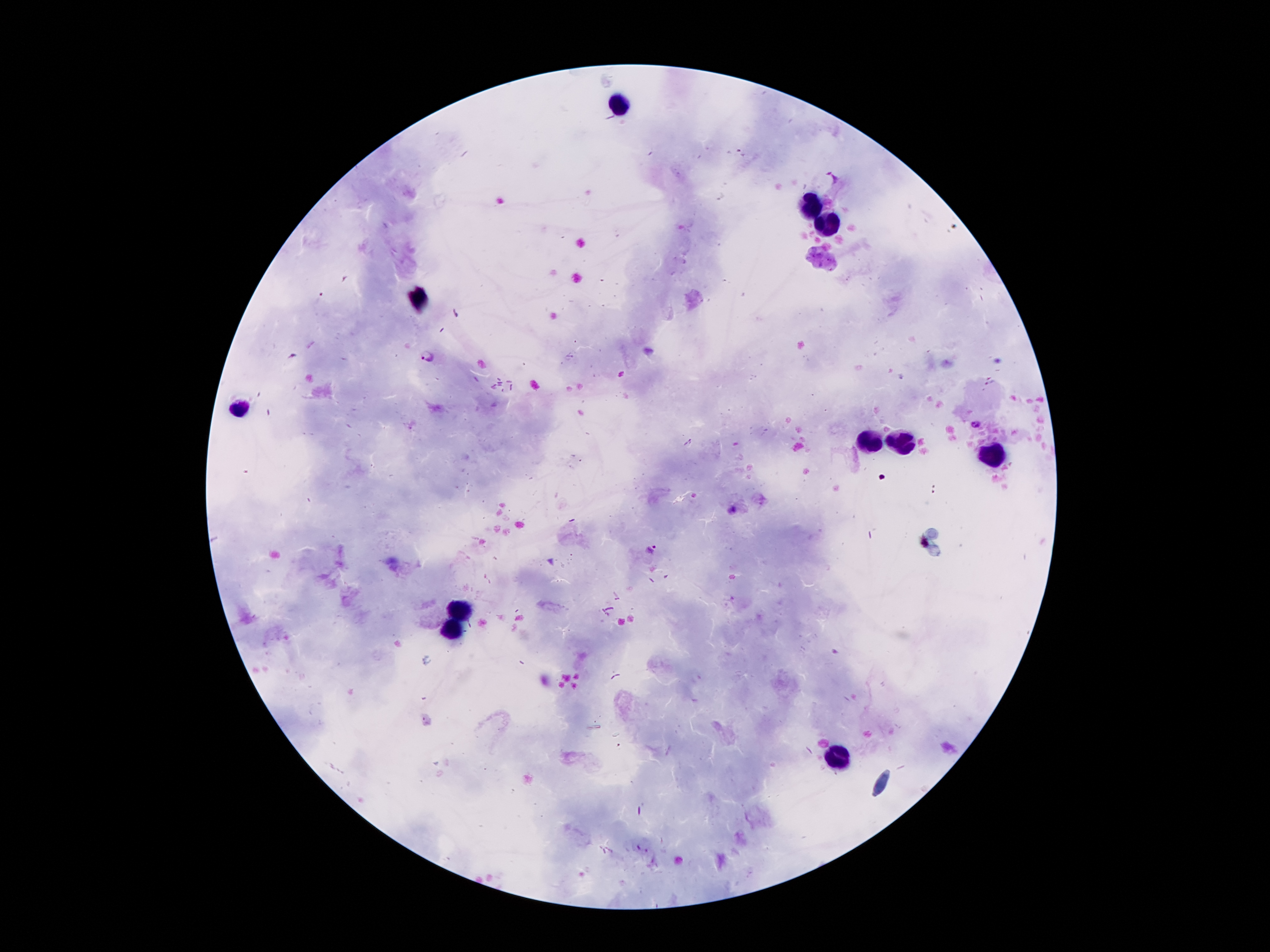 Approximate centers as {x, y} in pixels. Leukocyte locations: {626, 101}, {813, 204}, {828, 221}, {420, 298}, {244, 408}, {874, 443}, {903, 443}, {993, 454}, {461, 609}, {452, 630}, {841, 759}. Malaria parasite locations: {832, 178}, {428, 354}, {976, 423}, {652, 547}. Smartphone photograph taken through the microscope eyepiece. Single field of view. Patient malaria status: infected with Plasmodium falciparum. 100x magnification. Giemsa stain. Image is 1270×952 pixels. Thick peripheral-blood smear.